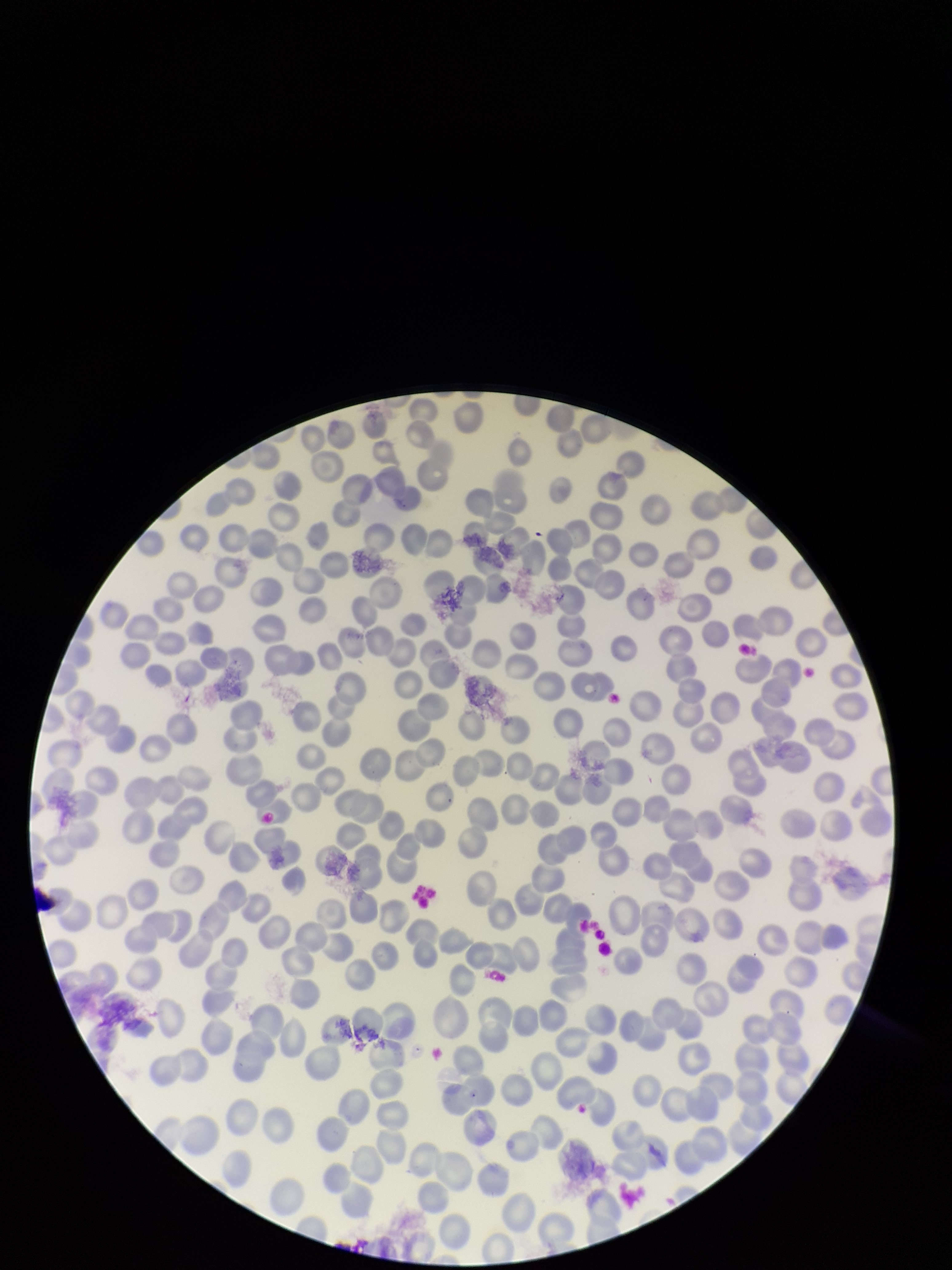
image size = 952×1270 pixels
capture = smartphone photograph through the microscope eyepiece
parasitized red blood cell count = 0
parasitized red blood cells = none detected
stain = Giemsa
patient malaria status = negative
field of view = single
preparation = thin smear
red blood cell count = 285